Describe the morphology of the erythrocytes.
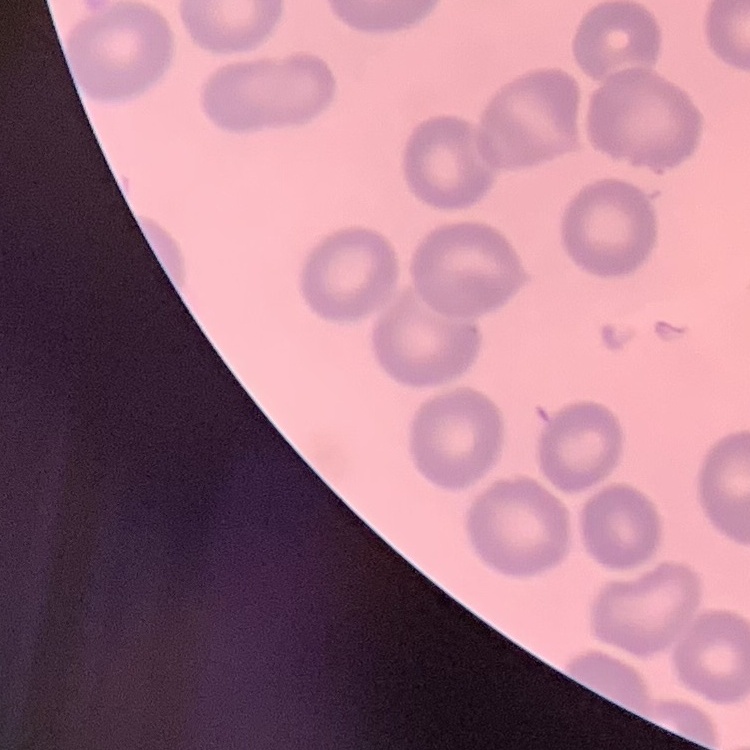

They show no rouleaux formation.

Thin blood film. Stained with either Field's or Giemsa. One tile cut from a larger photomicrograph.